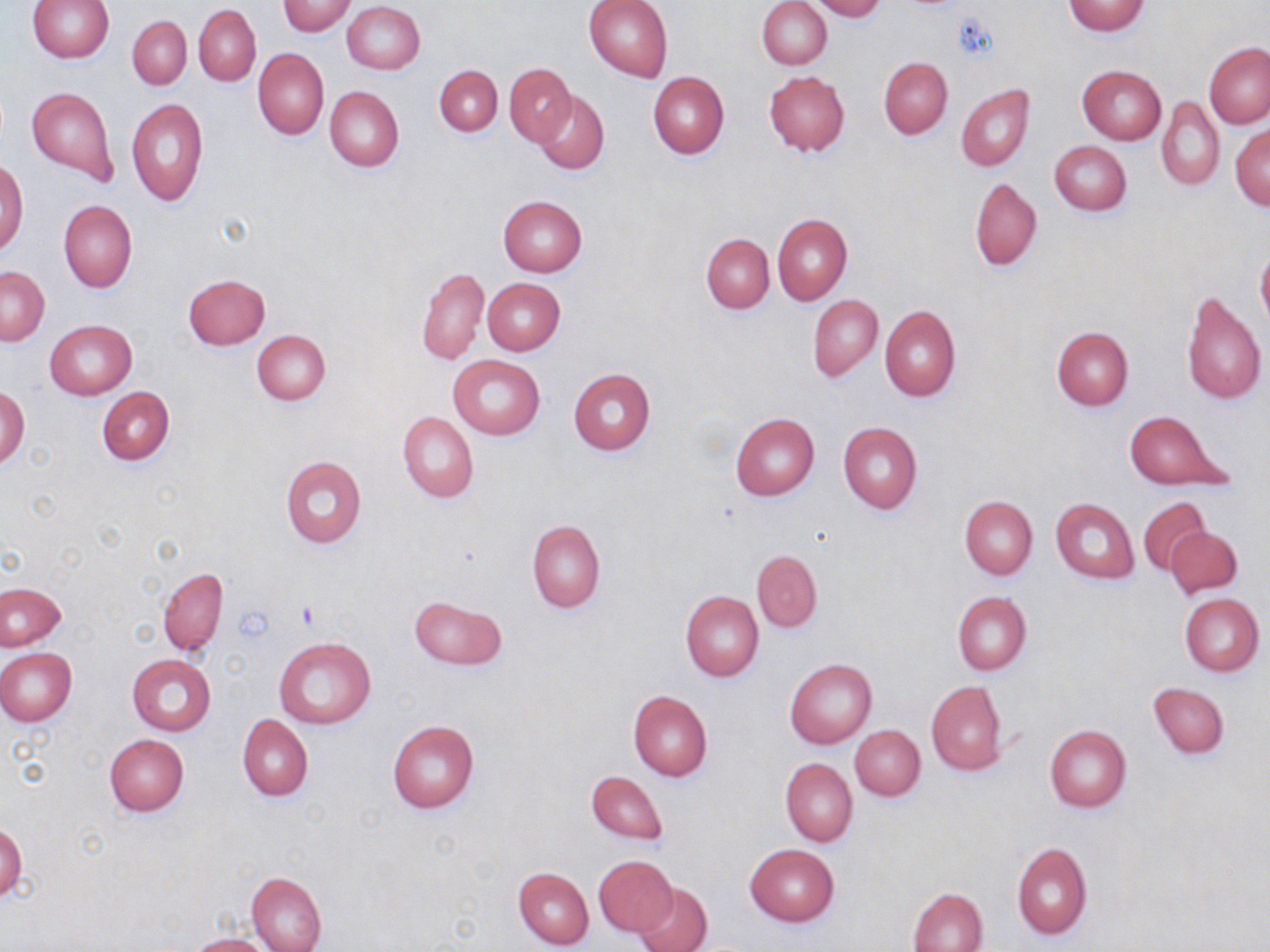
{
  "slide_level_diagnosis": "no evidence of blood parasites",
  "preparation": "thin blood smear",
  "stain": "May-Grünwald-Giemsa",
  "modality": "optical microscopy",
  "magnification": "1000x",
  "image_size": "1270×952 pixels",
  "uninfected_red_blood_cell_locations": "approximate bounding boxes as (x1,y1)-(x2,y2) corner pairs in pixels: (583,0)-(673,82), (810,0)-(886,21), (28,1)-(114,63), (279,1)-(356,36), (343,1)-(426,74), (758,1)-(831,69), (1063,1)-(1150,36), (194,4)-(261,86), (127,16)-(191,88), (1204,42)-(1270,129), (254,48)-(328,139), (879,57)-(952,139), (505,63)-(575,147), (434,65)-(502,136), (1078,65)-(1166,145), (764,71)-(850,155), (648,72)-(728,159), (955,84)-(1034,171), (26,86)-(119,183), (325,86)-(404,172), (535,92)-(609,174), (1156,97)-(1224,191), (127,98)-(208,207), (1230,123)-(1269,210), (1049,141)-(1131,216), (0,161)-(28,255), (970,177)-(1042,271), (498,195)-(587,276), (59,200)-(137,292), (773,213)-(851,305), (702,233)-(774,313), (1257,244)-(1270,331), (1,267)-(50,346), (417,268)-(488,365), (184,274)-(270,350), (482,277)-(565,355), (1180,290)-(1266,405), (808,295)-(883,382), (878,305)-(961,401), (45,319)-(136,400), (1051,327)-(1133,410), (252,330)-(330,406), (448,355)-(545,440), (568,367)-(655,455), (0,385)-(30,469), (98,386)-(175,466), (398,412)-(478,502), (730,412)-(819,501), (1126,412)-(1228,488), (837,422)-(922,514), (279,456)-(367,548), (959,495)-(1037,579), (1138,496)-(1211,575), (1050,498)-(1140,582), (527,520)-(605,612), (1165,526)-(1242,599), (752,549)-(822,632), (158,567)-(228,655), (0,582)-(66,651), (681,591)-(764,682), (952,592)-(1031,675), (1179,593)-(1265,676), (409,595)-(507,670), (274,637)-(376,728), (0,648)-(77,725), (126,654)-(216,735), (785,657)-(877,749), (925,681)-(1007,775), (1148,682)-(1228,757), (628,690)-(713,781), (238,715)-(313,800), (386,719)-(478,814), (1044,723)-(1131,813), (850,725)-(924,801), (104,733)-(189,816), (780,757)-(857,847), (587,769)-(667,847), (0,825)-(26,902), (1012,841)-(1092,941), (744,843)-(839,926), (593,854)-(678,937), (513,867)-(593,950), (246,872)-(327,952), (635,882)-(712,952), (908,887)-(989,952), (189,935)-(271,952)",
  "field_of_view": "one of a larger specimen",
  "platelet_locations": "approximate bounding boxes as (x1,y1)-(x2,y2) corner pairs in pixels: (953,11)-(996,62)"
}